Report the malaria status of this cell.
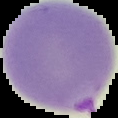

Parasitized.

{
  "image_size": "118×118 pixels",
  "preparation": "thin blood film",
  "image_type": "segmented cell region with the area outside set to black"
}